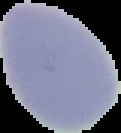

image size = 121×133 pixels
image type = segmented cell region with the area outside set to black
preparation = thin blood film
result = no malaria parasites detected